State the blood parasite species.
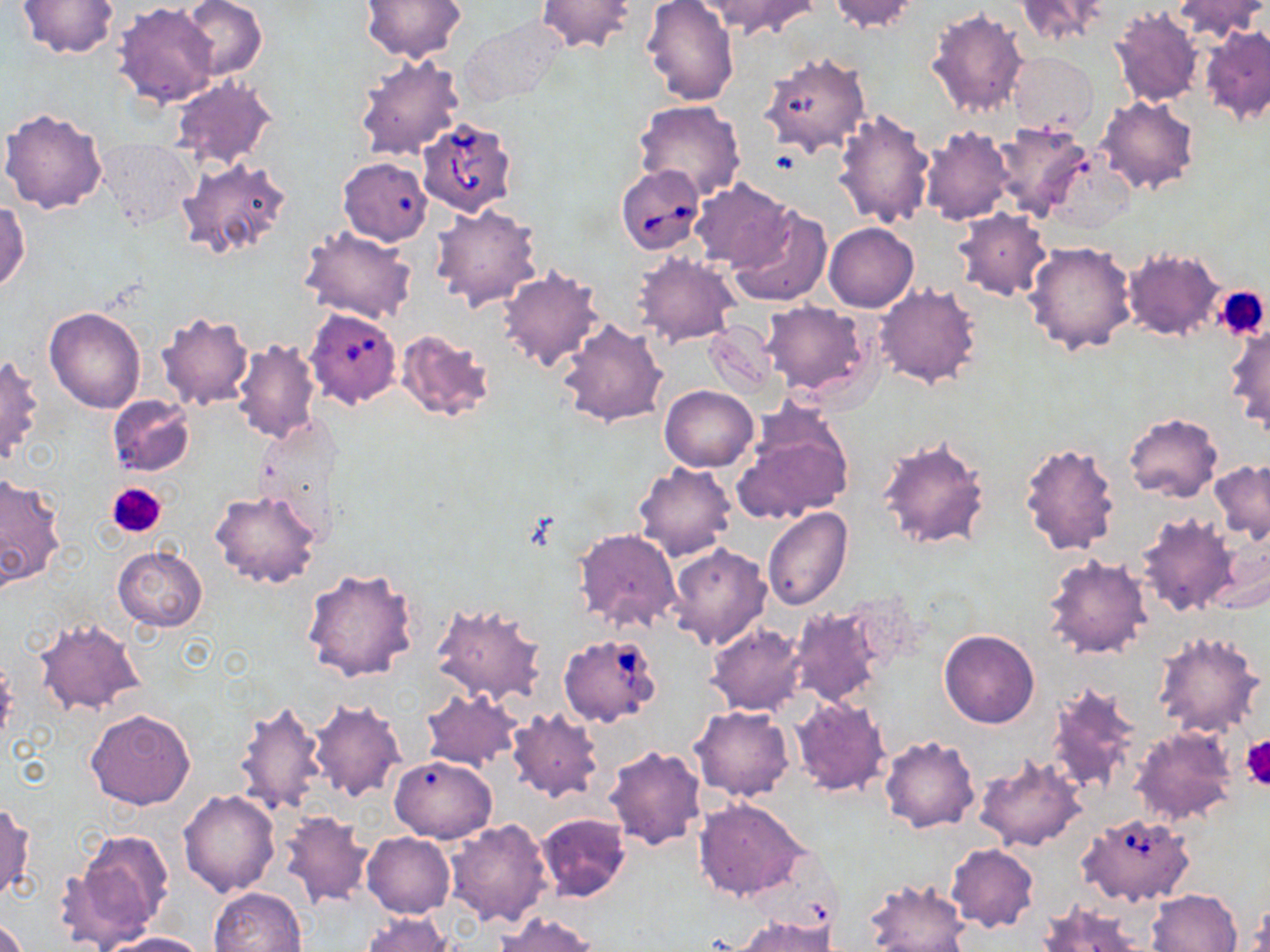

Babesia divergens.

Summary:
  - Coordinate format: approximate bounding boxes as (x1, y1, x2, y2) in pixels
  - Babesia divergens-infected red blood cell locations: (417, 116, 520, 218), (615, 164, 707, 255), (302, 306, 404, 415), (554, 635, 661, 727), (1077, 812, 1196, 907)
  - Uninfected red blood cell locations: (18, 0, 120, 58), (181, 0, 267, 80), (358, 0, 468, 62), (534, 0, 636, 54), (641, 0, 740, 105), (705, 0, 816, 38), (827, 0, 921, 33), (1013, 0, 1110, 46), (1172, 0, 1266, 41), (112, 2, 221, 110), (1107, 5, 1203, 107), (926, 6, 1029, 117), (457, 17, 568, 108), (1201, 26, 1270, 124), (1006, 51, 1098, 135), (353, 53, 463, 162), (762, 56, 869, 156), (169, 77, 277, 168), (1096, 95, 1200, 196), (632, 101, 747, 201), (832, 107, 935, 230), (1, 108, 108, 215), (989, 122, 1094, 221), (920, 127, 1014, 225), (98, 140, 196, 229), (178, 156, 291, 260), (333, 160, 435, 241), (688, 180, 795, 271), (0, 200, 30, 293), (430, 204, 542, 311), (729, 207, 832, 306), (952, 208, 1052, 301), (823, 222, 919, 312), (298, 227, 417, 324), (1023, 241, 1136, 356), (1123, 249, 1226, 342), (633, 253, 741, 346), (496, 268, 605, 373), (874, 283, 982, 389), (760, 301, 870, 394), (44, 307, 145, 412), (153, 310, 253, 411), (556, 318, 668, 428), (1225, 319, 1270, 436), (705, 322, 780, 398), (395, 330, 496, 423), (233, 339, 321, 444), (0, 353, 43, 466), (659, 385, 758, 472), (106, 395, 195, 477), (735, 410, 854, 522), (1124, 412, 1222, 501), (250, 415, 344, 534), (877, 435, 992, 552), (1018, 440, 1121, 557), (1208, 459, 1270, 544), (632, 462, 737, 561), (0, 473, 65, 591), (209, 489, 322, 589), (761, 508, 852, 611), (1134, 513, 1238, 617), (573, 528, 683, 635), (1205, 536, 1269, 616), (668, 543, 772, 651), (113, 546, 207, 632), (1042, 555, 1153, 661), (301, 566, 419, 685), (432, 601, 546, 704), (786, 605, 885, 709), (33, 619, 144, 716), (706, 624, 806, 717), (939, 629, 1039, 728), (1152, 631, 1265, 738), (1044, 681, 1142, 796), (419, 688, 523, 771), (791, 697, 891, 797), (308, 698, 406, 802), (233, 700, 327, 817), (691, 706, 793, 801), (84, 708, 194, 810), (506, 710, 605, 802), (1130, 726, 1237, 825), (880, 735, 979, 833), (603, 744, 709, 851), (974, 753, 1086, 851), (389, 755, 496, 842), (179, 790, 280, 897), (693, 799, 808, 900), (0, 802, 34, 902), (278, 810, 374, 908), (535, 812, 633, 902), (446, 818, 553, 925), (64, 828, 175, 950), (363, 833, 455, 918), (946, 843, 1039, 932), (862, 878, 970, 952), (209, 887, 307, 952), (1148, 888, 1242, 951), (1244, 900, 1268, 950), (1034, 901, 1147, 952), (363, 912, 453, 952), (493, 912, 599, 952), (735, 914, 836, 952), (0, 917, 29, 952), (100, 932, 208, 952)
  - Platelet locations: (1215, 285, 1269, 339), (105, 483, 167, 538), (1241, 735, 1270, 789)
  - Preparation: thin blood smear
  - Field of view: one of a larger specimen
  - Modality: light microscopy
  - Image size: 1270×952 pixels
  - Stain: May-Grünwald-Giemsa
  - Magnification: 1000x